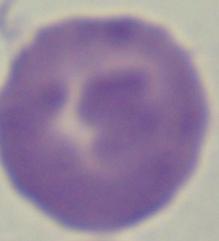
Summary:
  - Modality: micrograph
  - Magnification: 1000x
  - Identification: Babesia